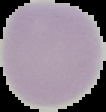
Summary:
  - Malaria status: uninfected
  - Preparation: thin blood smear
  - Image size: 106×112 pixels
  - Image type: segmented cell region with the area outside set to black